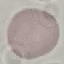
malaria status = uninfected
image type = cell patch, automatically extracted from a larger field of view and resized to 64 × 64 pixels
capture = smartphone camera at the microscope eyepiece
stain = Giemsa
preparation = thin smear